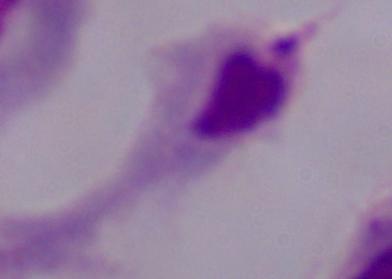

modality = micrograph
magnification = 1000x
identification = trichomonad